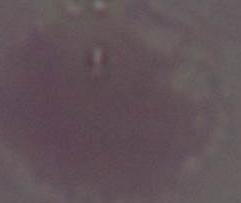
{
  "modality": "micrograph",
  "identification": "red blood cell",
  "magnification": "1000x"
}